Classify this cell by malaria status.
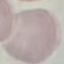
It is uninfected.

{
  "stain": "Giemsa",
  "preparation": "thin blood film",
  "capture": "smartphone through the microscope eyepiece",
  "image_type": "cell patch, automatically extracted from a larger field of view and resized to 64 × 64 pixels"
}